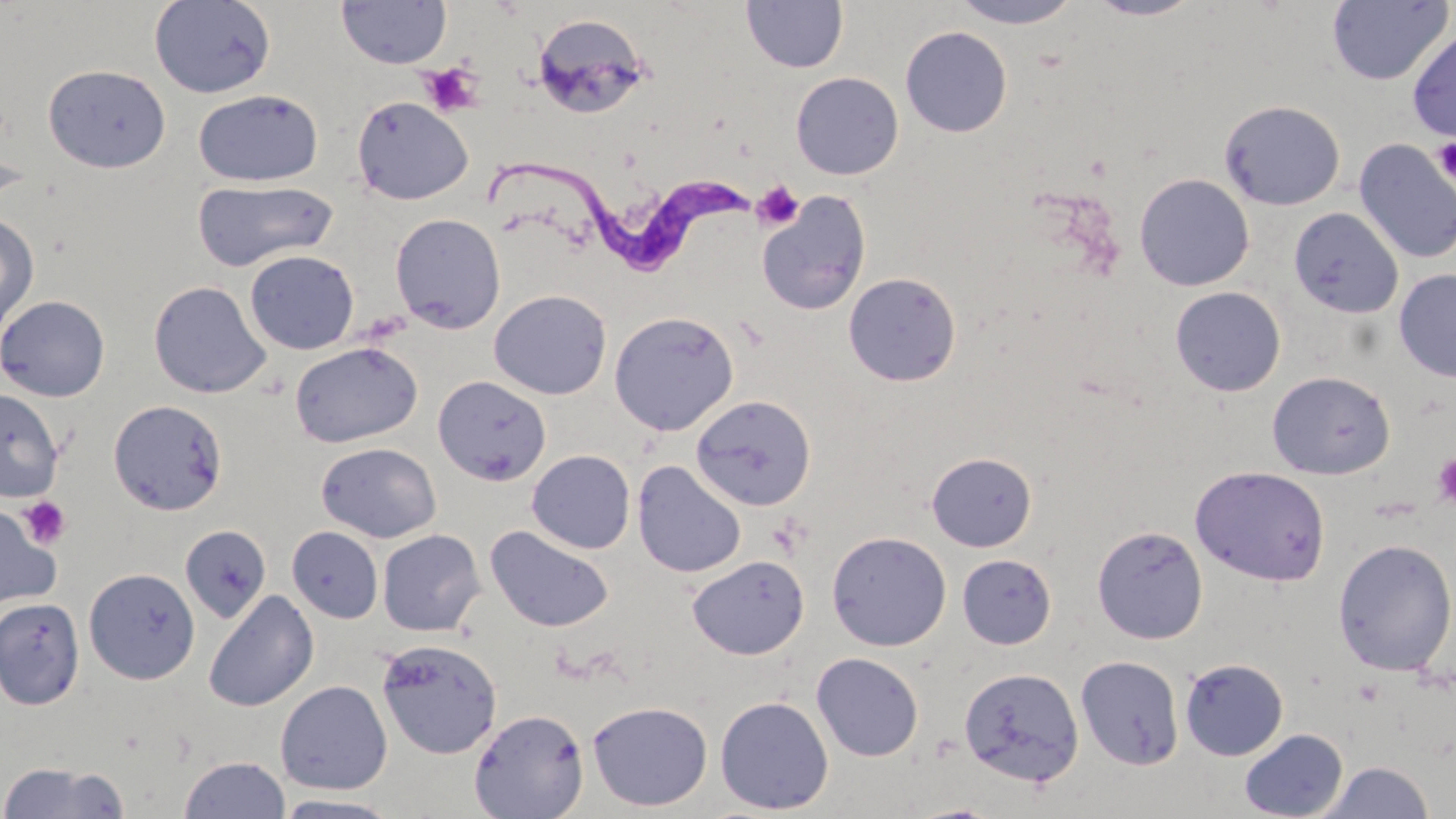 Approximate bounding boxes as named x1/y1/x2/y2 corners in pixels. Trypanosoma brucei locations: (x1=476, y1=159, x2=756, y2=273). Uninfected red blood cell locations: (x1=741, y1=0, x2=848, y2=73), (x1=947, y1=0, x2=1086, y2=29), (x1=1085, y1=0, x2=1205, y2=21), (x1=1327, y1=0, x2=1452, y2=86), (x1=148, y1=1, x2=276, y2=98), (x1=336, y1=1, x2=452, y2=69), (x1=532, y1=13, x2=651, y2=120), (x1=900, y1=26, x2=1012, y2=137), (x1=1406, y1=28, x2=1456, y2=142), (x1=43, y1=64, x2=171, y2=173), (x1=790, y1=72, x2=904, y2=180), (x1=193, y1=89, x2=324, y2=187), (x1=351, y1=96, x2=473, y2=205), (x1=1218, y1=99, x2=1346, y2=211), (x1=1353, y1=139, x2=1456, y2=264), (x1=1134, y1=173, x2=1255, y2=292), (x1=193, y1=179, x2=339, y2=272), (x1=756, y1=191, x2=872, y2=316), (x1=1290, y1=207, x2=1404, y2=319), (x1=0, y1=211, x2=40, y2=336), (x1=390, y1=213, x2=506, y2=334), (x1=244, y1=250, x2=360, y2=355), (x1=1394, y1=269, x2=1456, y2=382), (x1=843, y1=272, x2=962, y2=387), (x1=148, y1=280, x2=271, y2=398), (x1=1170, y1=286, x2=1286, y2=397), (x1=489, y1=289, x2=612, y2=400), (x1=0, y1=295, x2=110, y2=402), (x1=489, y1=299, x2=735, y2=411), (x1=609, y1=311, x2=740, y2=436), (x1=289, y1=341, x2=422, y2=447), (x1=1267, y1=370, x2=1395, y2=479), (x1=433, y1=375, x2=552, y2=486), (x1=0, y1=388, x2=64, y2=503), (x1=691, y1=394, x2=817, y2=510), (x1=108, y1=399, x2=228, y2=516), (x1=316, y1=442, x2=441, y2=543), (x1=526, y1=450, x2=635, y2=554), (x1=927, y1=452, x2=1036, y2=552), (x1=632, y1=459, x2=746, y2=579), (x1=1190, y1=465, x2=1330, y2=586), (x1=0, y1=503, x2=61, y2=613), (x1=484, y1=524, x2=614, y2=633), (x1=1092, y1=524, x2=1208, y2=645), (x1=180, y1=525, x2=271, y2=624), (x1=288, y1=526, x2=383, y2=623), (x1=377, y1=529, x2=485, y2=636), (x1=827, y1=531, x2=951, y2=651), (x1=1333, y1=538, x2=1456, y2=676), (x1=957, y1=554, x2=1056, y2=648), (x1=688, y1=555, x2=809, y2=659), (x1=83, y1=567, x2=201, y2=685), (x1=203, y1=589, x2=320, y2=712), (x1=0, y1=597, x2=85, y2=710), (x1=376, y1=638, x2=503, y2=759), (x1=811, y1=652, x2=923, y2=761), (x1=1076, y1=655, x2=1185, y2=769), (x1=1179, y1=657, x2=1288, y2=760), (x1=959, y1=666, x2=1084, y2=787), (x1=275, y1=680, x2=392, y2=795), (x1=715, y1=695, x2=834, y2=815), (x1=587, y1=700, x2=713, y2=812), (x1=468, y1=708, x2=589, y2=819), (x1=1239, y1=728, x2=1349, y2=819), (x1=179, y1=755, x2=291, y2=819), (x1=0, y1=760, x2=130, y2=818), (x1=1319, y1=760, x2=1435, y2=819), (x1=271, y1=794, x2=403, y2=818). Platelet locations: (x1=419, y1=62, x2=485, y2=117), (x1=1431, y1=135, x2=1456, y2=188), (x1=752, y1=181, x2=804, y2=231), (x1=1431, y1=453, x2=1456, y2=509), (x1=17, y1=496, x2=73, y2=549). Slide-level diagnosis: Trypanosoma brucei. Optical microscopy. One field of a larger specimen. 1000x magnification. May-Grünwald-Giemsa stain. Image is 1456×819 pixels. Thin blood film.